Locate every Plasmodium ovale-infected red blood cell.
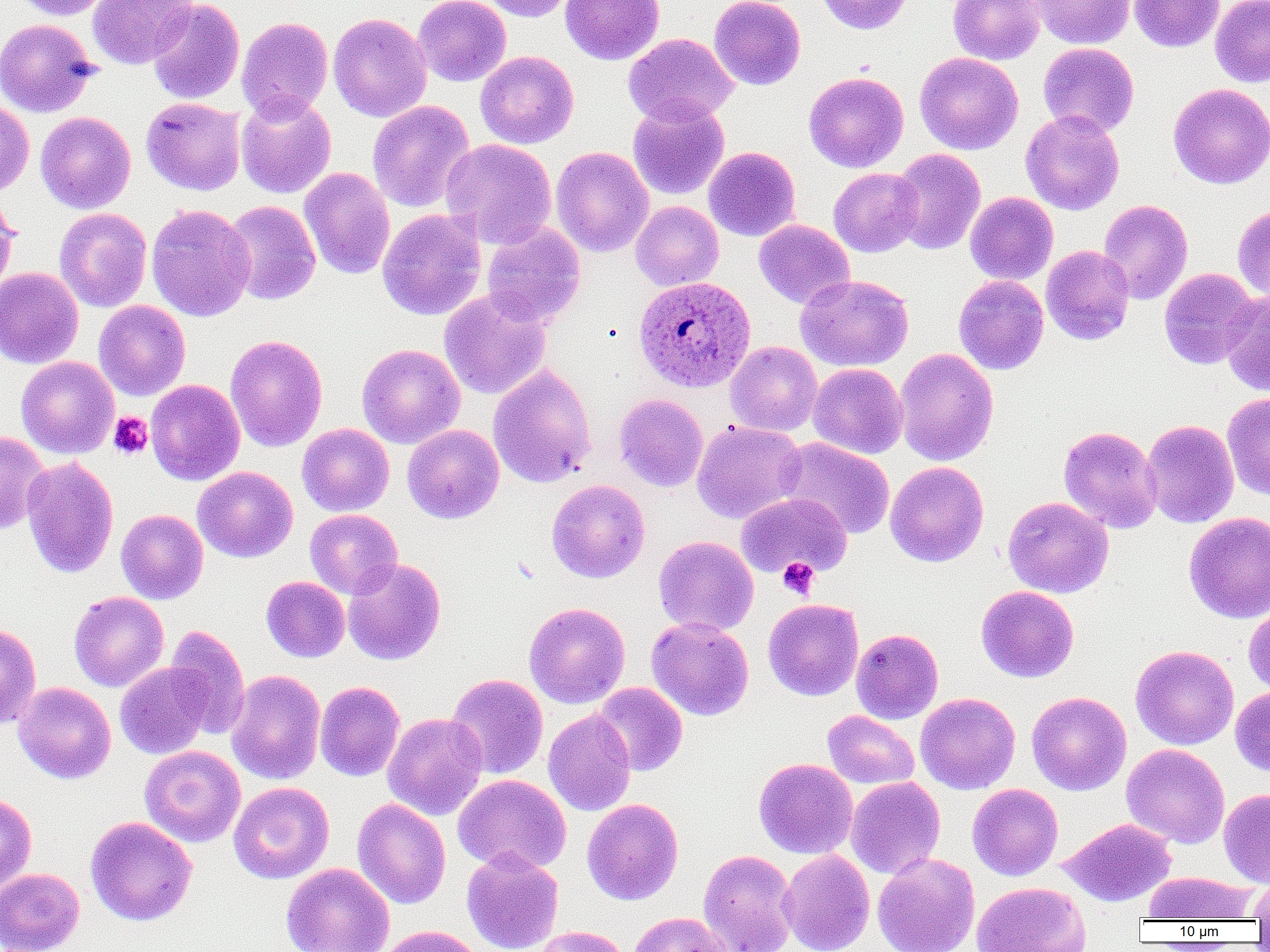

Approximate bounding boxes as (x1, y1, x2, y2) in pixels.
Plasmodium ovale-infected red blood cells: (636, 277, 758, 394).

Summary:
  - Uninfected red blood cell locations: (8, 0, 115, 20), (87, 0, 198, 69), (413, 0, 511, 87), (479, 0, 578, 22), (560, 0, 664, 65), (709, 0, 806, 90), (815, 0, 915, 35), (948, 0, 1045, 65), (1030, 0, 1135, 48), (1130, 0, 1224, 52), (1210, 0, 1270, 87), (147, 1, 245, 104), (328, 12, 431, 122), (236, 16, 333, 121), (0, 18, 99, 117), (624, 33, 738, 126), (1038, 42, 1139, 136), (475, 50, 579, 149), (915, 52, 1024, 155), (804, 71, 909, 172), (1168, 83, 1270, 189), (236, 93, 336, 199), (141, 97, 246, 195), (627, 98, 729, 199), (0, 99, 34, 197), (367, 100, 475, 213), (1021, 110, 1125, 215), (36, 111, 136, 213), (440, 138, 557, 248), (551, 146, 653, 257), (704, 147, 801, 241), (891, 148, 986, 255), (300, 167, 396, 279), (828, 167, 923, 257), (965, 192, 1058, 285), (0, 194, 19, 297), (1098, 199, 1193, 304), (222, 200, 321, 305), (630, 200, 724, 291), (1233, 202, 1270, 303), (146, 204, 256, 321), (54, 208, 152, 312), (377, 209, 486, 320), (753, 219, 856, 309), (482, 222, 585, 328), (1040, 245, 1135, 345), (0, 267, 84, 368), (1159, 268, 1259, 369), (796, 274, 913, 371), (953, 275, 1049, 374), (439, 289, 551, 399), (1220, 291, 1270, 397), (93, 300, 190, 400), (226, 335, 327, 451), (725, 341, 822, 436), (357, 343, 465, 449), (894, 347, 998, 466), (16, 356, 119, 458), (808, 363, 908, 459), (488, 364, 597, 488), (146, 379, 245, 485), (1222, 392, 1270, 502), (613, 393, 708, 492), (1141, 419, 1239, 528), (691, 420, 806, 524), (297, 423, 394, 516), (402, 424, 504, 524), (1058, 425, 1162, 533), (0, 431, 49, 535), (776, 437, 896, 539), (21, 457, 119, 578), (885, 461, 988, 567), (192, 466, 298, 562), (547, 479, 650, 583), (736, 492, 851, 579), (1003, 496, 1114, 598), (116, 509, 208, 604), (305, 509, 402, 599), (1184, 511, 1270, 622), (653, 536, 758, 636), (343, 558, 446, 665), (261, 576, 350, 662), (976, 586, 1079, 682), (69, 591, 169, 692), (763, 599, 864, 701), (524, 602, 630, 709), (1243, 603, 1270, 696), (646, 617, 754, 721), (0, 622, 41, 729), (164, 624, 250, 740), (851, 628, 944, 724), (1131, 645, 1239, 750), (115, 662, 213, 759), (226, 669, 326, 785), (445, 673, 548, 779), (315, 681, 405, 781), (13, 682, 116, 784), (592, 683, 687, 776), (1230, 686, 1270, 777), (1026, 691, 1131, 795), (915, 692, 1020, 794), (543, 709, 636, 816), (822, 710, 919, 790), (383, 713, 488, 820), (1121, 743, 1230, 848), (139, 745, 245, 847), (754, 758, 858, 859), (452, 774, 571, 874), (846, 777, 945, 879), (228, 781, 334, 884), (967, 783, 1063, 880), (1219, 788, 1270, 888), (0, 792, 37, 894), (352, 798, 451, 909), (582, 798, 683, 905), (85, 817, 197, 926), (1059, 818, 1177, 906), (461, 848, 563, 952), (698, 849, 798, 952), (778, 849, 875, 952), (873, 853, 980, 952), (281, 862, 394, 952), (0, 868, 85, 952), (1142, 871, 1256, 922), (1248, 875, 1270, 922), (971, 881, 1091, 952), (629, 912, 733, 952), (376, 925, 484, 952), (532, 926, 631, 952)
  - Platelet locations: (108, 411, 153, 459), (778, 558, 819, 598)
  - Slide-level diagnosis: Plasmodium ovale
  - Modality: light microscopy
  - Preparation: thin blood film
  - Image size: 1270×952 pixels
  - Field of view: one of a larger specimen
  - Magnification: 1000x